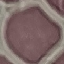
result = no malaria parasites seen
stain = Giemsa
capture = smartphone through the microscope eyepiece
image type = cell patch, automatically extracted from a larger field of view and resized to 64 × 64 pixels
preparation = thin blood smear